Name the blood parasite species.
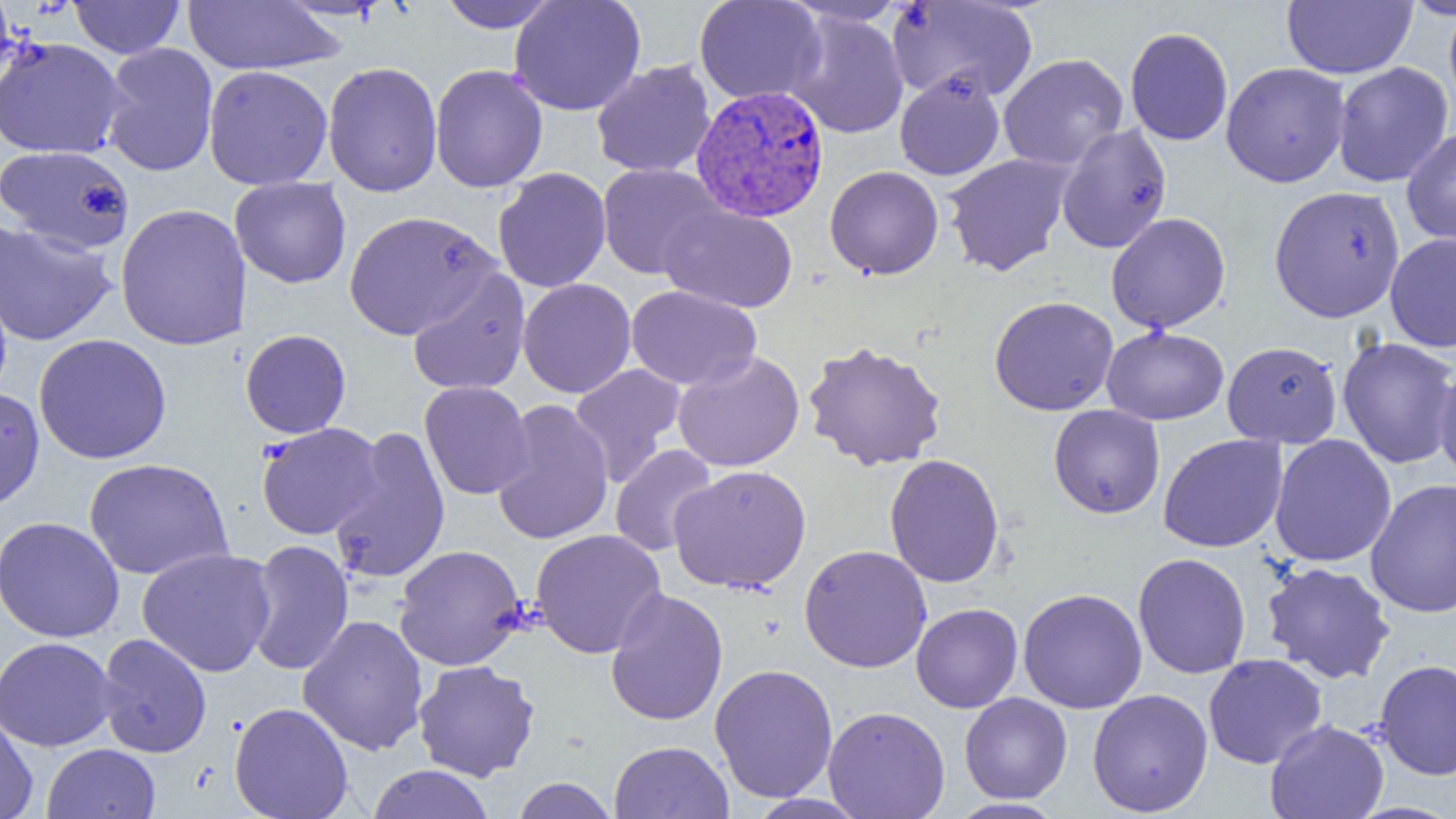
Plasmodium vivax.

modality = light microscopy
Plasmodium vivax-infected red blood cell locations = approximate bounding boxes as (x1,y1)-(x2,y2) corner pairs in pixels: (691,85)-(829,223)
field of view = single
magnification = 1000x
uninfected red blood cell locations = approximate bounding boxes as (x1,y1)-(x2,y2) corner pairs in pixels: (0,0)-(17,92), (69,0)-(184,59), (435,0)-(560,32), (509,0)-(646,116), (694,0)-(826,105), (1282,0)-(1417,78), (1400,0)-(1456,20), (183,1)-(346,75), (887,1)-(1038,103), (784,10)-(909,139), (1125,27)-(1233,146), (0,37)-(126,159), (101,43)-(218,176), (998,53)-(1129,172), (592,59)-(716,178), (322,61)-(443,197), (1332,61)-(1453,187), (1220,62)-(1350,187), (430,64)-(548,193), (203,65)-(333,190), (894,70)-(1006,180), (1056,123)-(1172,254), (1401,126)-(1456,248), (1,144)-(135,253), (942,153)-(1075,276), (597,163)-(725,279), (825,165)-(944,280), (493,167)-(612,293), (229,177)-(351,288), (1268,185)-(1406,323), (115,202)-(252,351), (659,204)-(798,313), (344,209)-(499,339), (1106,212)-(1230,333), (0,220)-(117,346), (1385,233)-(1456,352), (406,266)-(531,396), (518,278)-(637,398), (625,285)-(761,391), (989,296)-(1119,416), (1101,326)-(1229,425), (240,329)-(351,438), (33,333)-(172,464), (1337,337)-(1456,469), (802,340)-(948,471), (1222,341)-(1342,448), (673,350)-(804,472), (569,363)-(687,485), (1433,363)-(1456,487), (419,380)-(534,500), (0,387)-(45,511), (492,399)-(614,545), (1048,404)-(1165,518), (256,422)-(385,540), (329,426)-(450,585), (1158,433)-(1287,553), (1269,434)-(1396,567), (610,444)-(719,557), (884,454)-(1005,588), (84,458)-(234,581), (669,464)-(812,593), (1365,479)-(1456,618), (0,516)-(124,642), (530,529)-(666,659), (244,539)-(355,677), (393,544)-(527,671), (799,544)-(932,673), (137,547)-(277,677), (1132,552)-(1251,679), (1261,561)-(1396,684), (605,587)-(729,726), (1018,587)-(1147,714), (911,603)-(1023,713), (297,614)-(429,756), (96,633)-(212,758), (0,636)-(118,751), (1203,653)-(1327,769), (1374,659)-(1456,780), (413,660)-(540,781), (710,662)-(838,803), (1087,688)-(1213,816), (959,693)-(1072,803), (229,701)-(354,819), (823,706)-(950,818), (0,711)-(39,819), (1265,719)-(1389,819), (609,740)-(734,819), (41,743)-(161,819), (365,764)-(495,819), (510,777)-(618,819), (745,793)-(869,819), (948,798)-(1066,818)
image size = 1456×819 pixels
preparation = thin blood smear